Identify the cell.
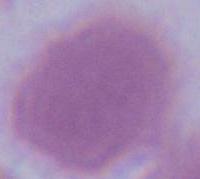

This is an erythrocyte.

1000x magnification. Photomicrograph.